Classify this cell by malaria status.
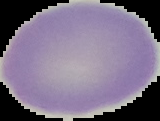
It is uninfected.

image type = cell region segmented out of the field of view; surrounding area masked to black
image size = 160×121 pixels
preparation = thin blood smear